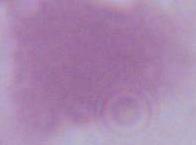
magnification = 1000x
identification = erythrocyte
modality = micrograph